Locate platelets.
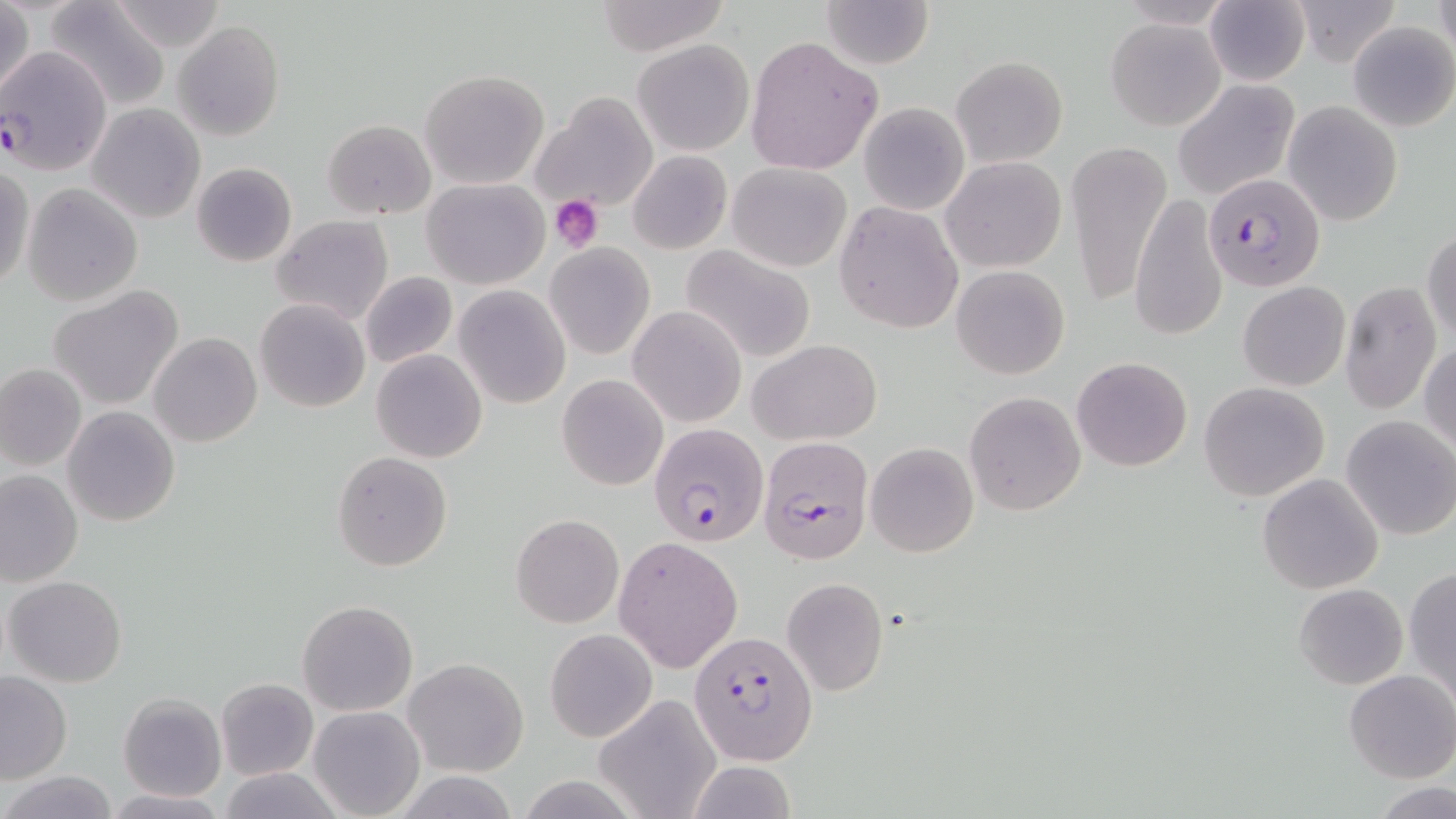
Approximate bounding boxes as (x1,y1)-(x2,y2) corner pairs in pixels.
Platelets: (551,197)-(603,251).

Summary:
  - Uninfected red blood cell locations: (106,0)-(227,52), (592,0)-(732,55), (819,0)-(936,70), (1290,0)-(1402,67), (43,1)-(171,110), (1433,1)-(1456,59), (1,2)-(35,104), (1204,2)-(1308,85), (1106,17)-(1224,129), (174,19)-(284,141), (1348,21)-(1456,131), (744,35)-(882,176), (633,39)-(754,156), (951,56)-(1068,168), (419,69)-(549,190), (1171,79)-(1300,200), (532,92)-(659,216), (859,102)-(969,215), (1283,102)-(1403,225), (87,104)-(205,223), (322,118)-(436,220), (1067,139)-(1172,307), (628,150)-(731,254), (941,156)-(1067,274), (191,162)-(296,267), (727,163)-(851,272), (0,164)-(34,290), (423,179)-(548,289), (22,183)-(143,305), (1130,192)-(1228,344), (834,201)-(963,334), (271,214)-(394,325), (1423,227)-(1456,345), (546,243)-(654,359), (681,245)-(816,363), (952,264)-(1071,379), (360,271)-(458,368), (1237,282)-(1350,390), (1339,282)-(1441,415), (454,285)-(570,408), (48,286)-(185,410), (254,299)-(370,413), (629,304)-(746,427), (150,332)-(261,447), (747,339)-(881,445), (1420,340)-(1455,455), (372,350)-(487,463), (1072,355)-(1192,471), (1,364)-(86,470), (557,373)-(668,491), (1199,381)-(1330,502), (963,391)-(1086,515), (62,406)-(179,527), (1341,416)-(1456,540), (865,442)-(978,556), (332,451)-(453,571), (0,471)-(82,587), (1257,473)-(1384,593), (511,513)-(623,628), (613,537)-(741,672), (1405,567)-(1456,704), (5,576)-(128,687), (780,577)-(888,696), (1294,583)-(1407,690), (297,600)-(418,716), (545,628)-(657,743), (403,658)-(528,777), (0,670)-(72,783), (1343,670)-(1456,783), (217,678)-(317,780), (118,694)-(225,800), (594,694)-(722,819), (308,705)-(425,819), (686,760)-(798,818), (215,766)-(344,819), (2,769)-(119,818), (1374,782)-(1456,818), (101,790)-(230,818)
  - Plasmodium falciparum-infected red blood cell locations: (0,42)-(114,172), (1204,171)-(1323,291), (650,422)-(770,546), (753,436)-(873,566), (688,631)-(816,763)
  - Slide-level diagnosis: Plasmodium falciparum
  - Stain: May-Grünwald-Giemsa
  - Preparation: thin blood smear
  - Field of view: one of a larger specimen
  - Modality: optical microscopy
  - Image size: 1456×819 pixels
  - Magnification: 1000x